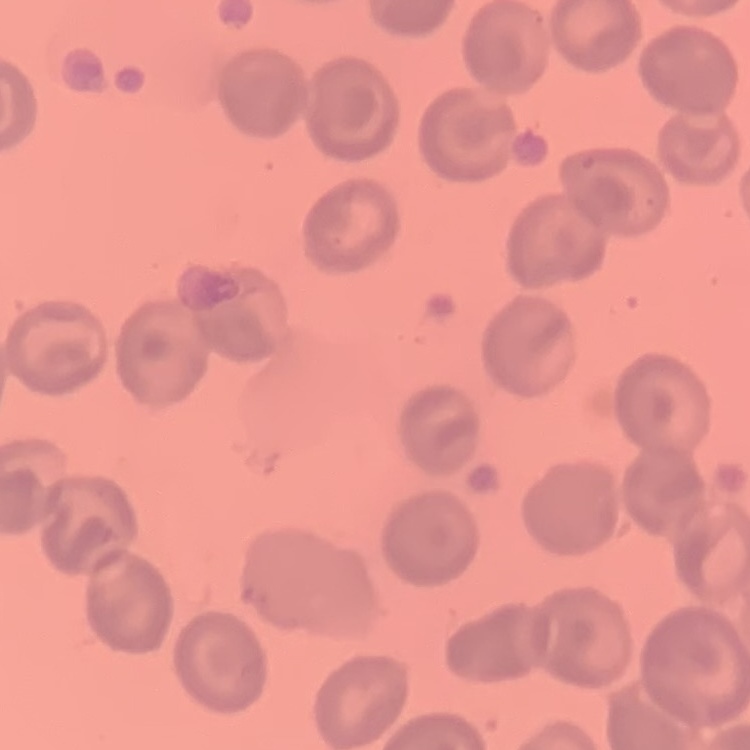
Summary:
  - Red blood cell morphology: no rouleaux formation
  - Image type: one tile cut from a larger photomicrograph
  - Stain: Field's or Giemsa
  - Preparation: thin blood smear